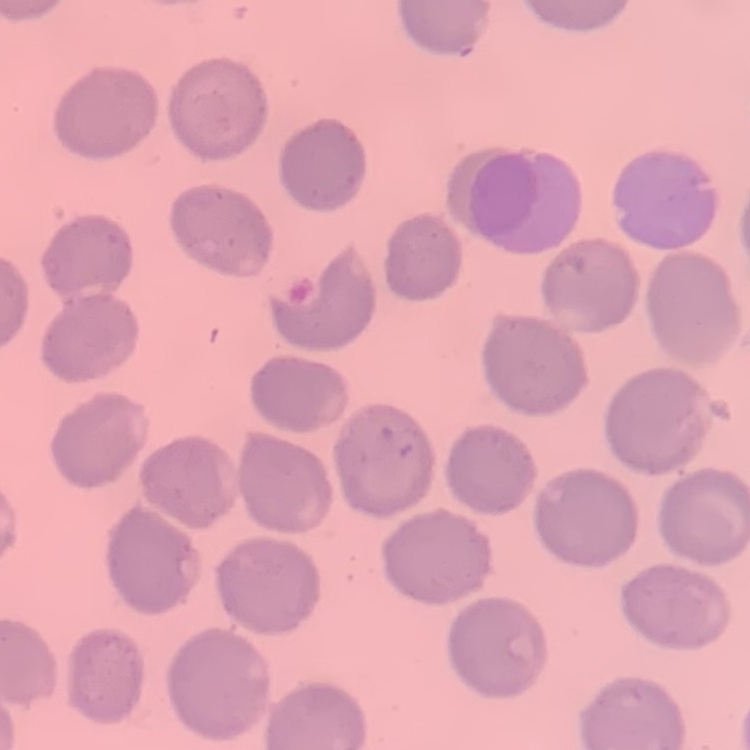

Summary:
  - Red blood cell morphology: no rouleaux formation
  - Preparation: thin blood smear
  - Stain: Field's or Giemsa
  - Image type: one tile cut from a larger photomicrograph